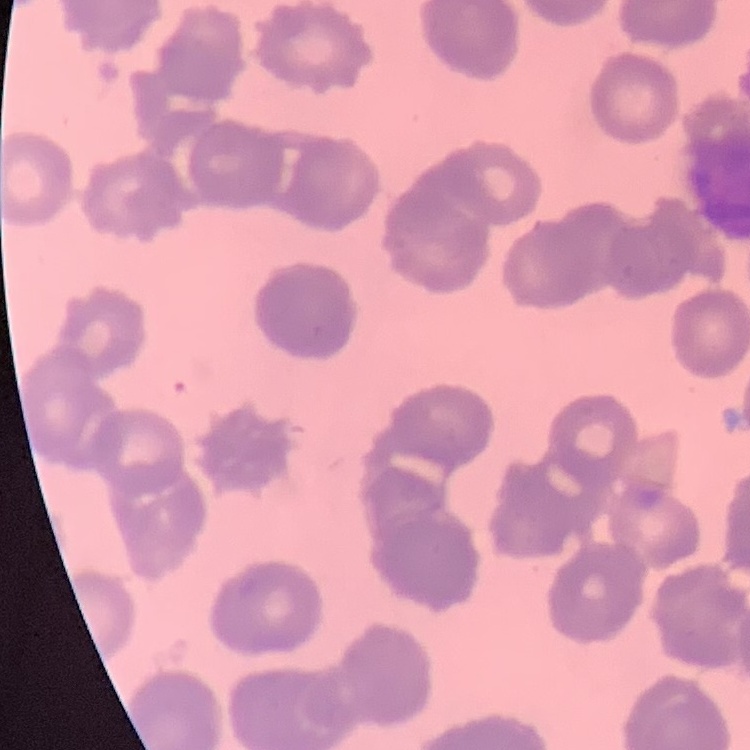

The erythrocytes show rouleaux formation. Thin blood film. One tile cut from a larger photomicrograph. Stained with either Field's or Giemsa.